Report the malaria status of this cell.
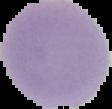
It is uninfected.

image size = 112×109 pixels
preparation = thin blood smear
image type = segmented cell region on a black background